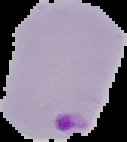

Image is 127×142 pixels. From a thin blood smear. Result: malaria parasites identified. Cell region segmented out of the field of view; the surrounding area is masked to black.